Assess the morphology of the red blood cells.
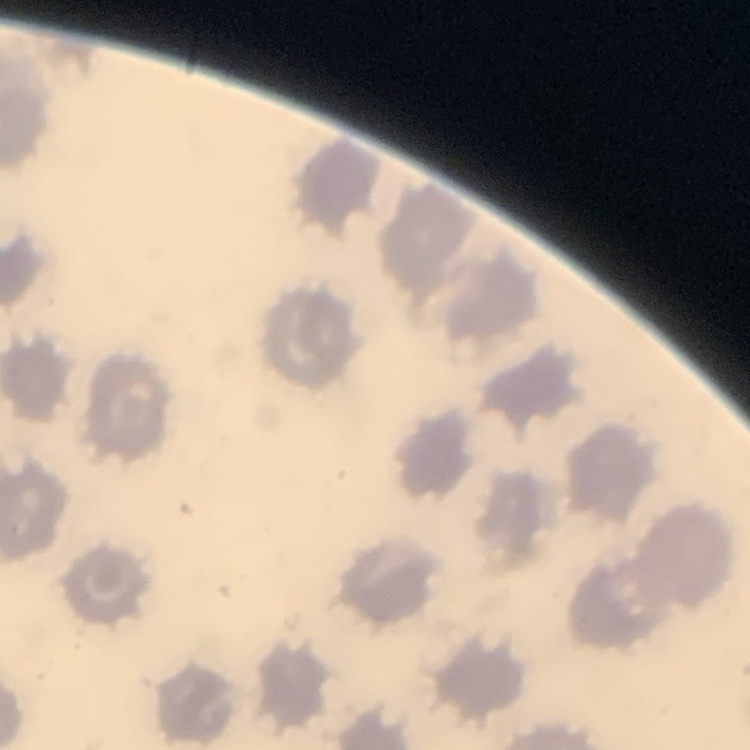
They show no rouleaux formation.

Summary:
  - Preparation: thin blood film
  - Stain: Field's or Giemsa
  - Image type: one tile cut from a larger photomicrograph